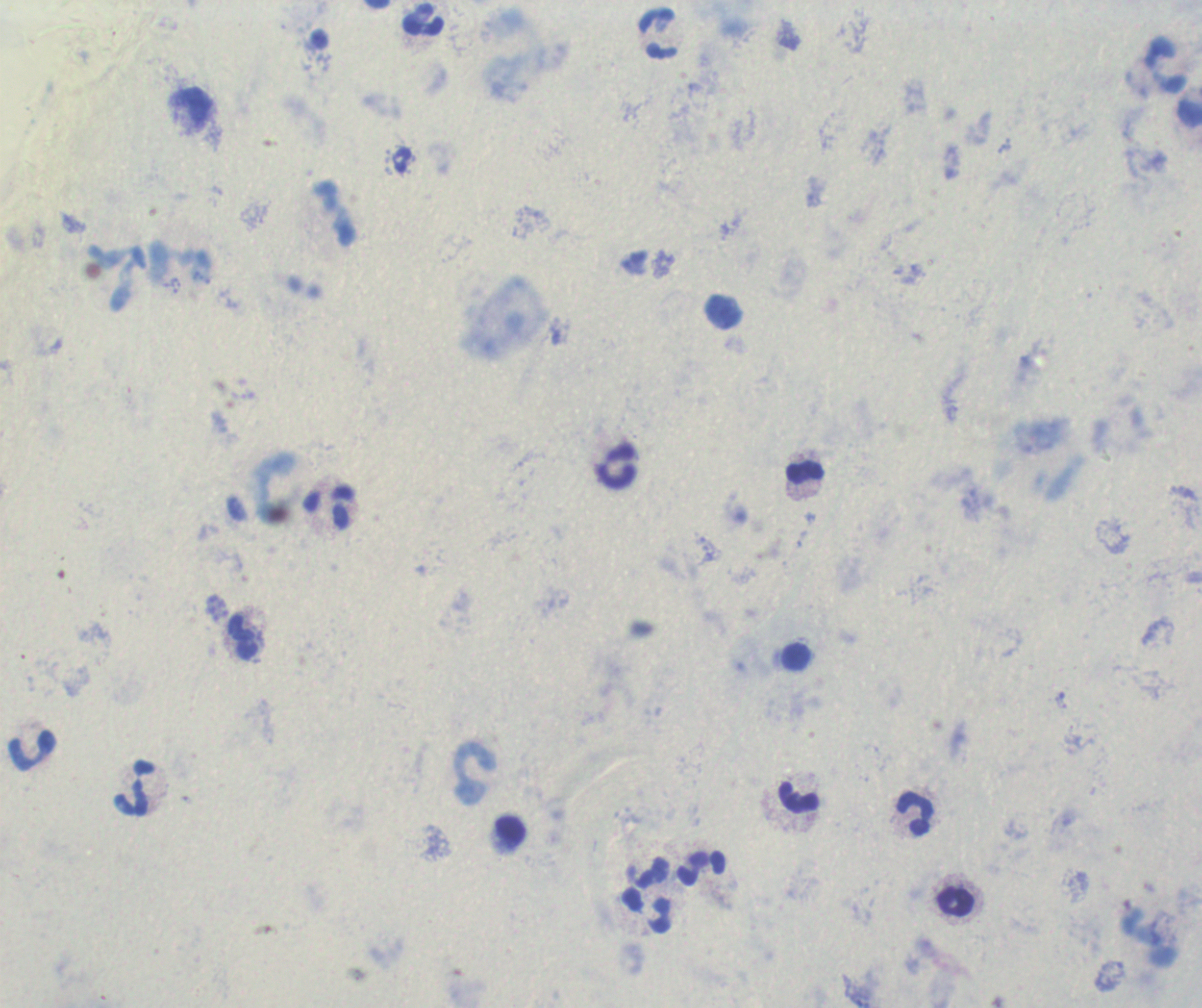 Approximate centers as {x, y} in pixels. Leukocyte locations: {423, 19}, {659, 34}, {1166, 65}, {191, 108}, {119, 279}, {615, 466}, {804, 471}, {329, 507}, {242, 636}, {795, 657}, {30, 751}, {473, 773}, {135, 788}, {799, 797}, {916, 814}, {511, 831}, {702, 868}, {648, 874}, {954, 902}, {647, 910}. Romanowsky-stained preparation. One field from this slide. Captured at 100x magnification. Thick blood film. Image is 1202×1008 pixels. Background quality: unsatisfactory. Result: no malaria parasites seen. Previously used in a real diagnosis.